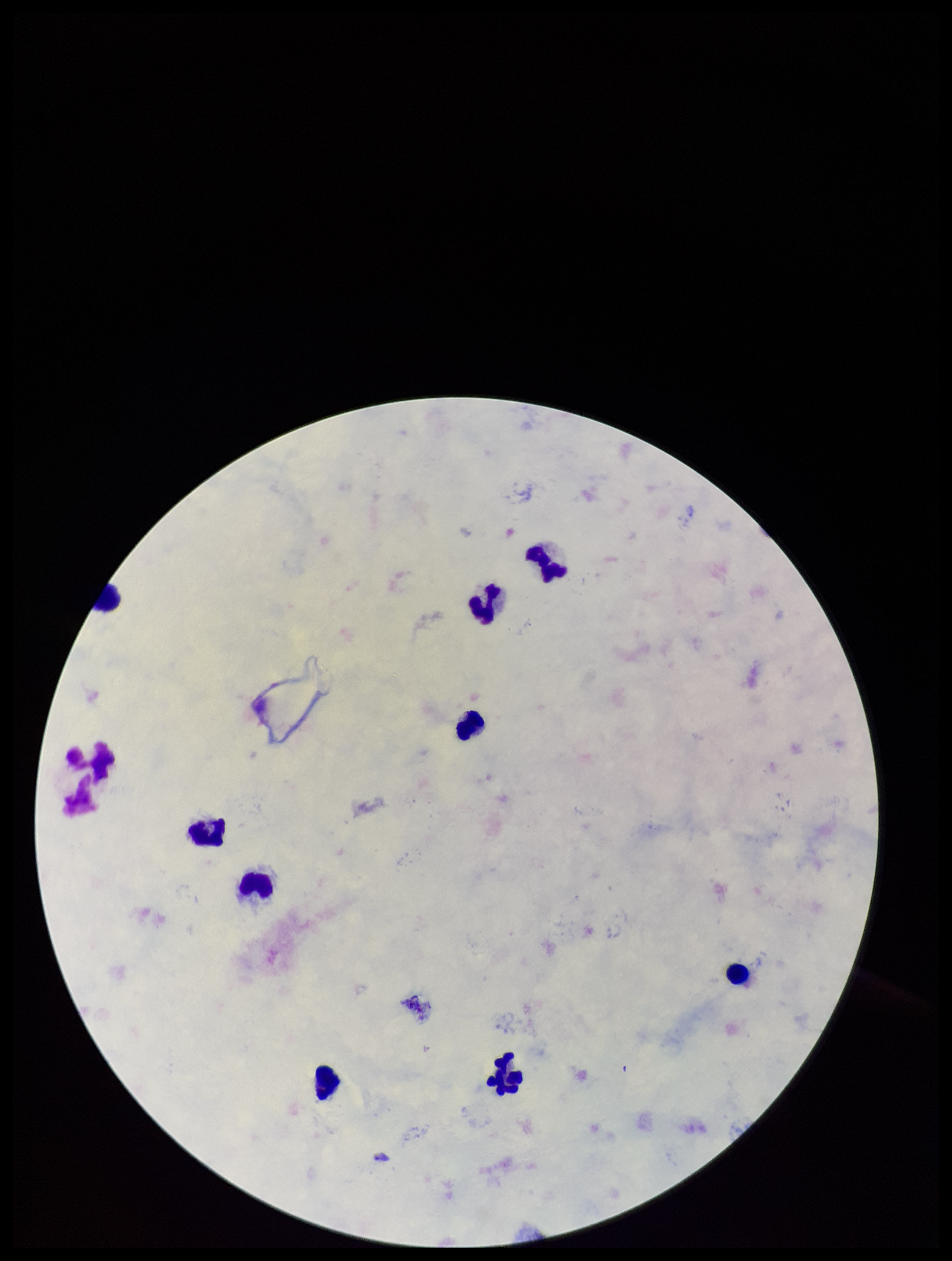
Plasmodium parasites = none seen
parasite count = 0
leukocyte count = 9
species reported for this patient = Plasmodium falciparum
capture = smartphone photograph through the microscope eyepiece
preparation = thick blood smear
image size = 952×1261 pixels
stain = Giemsa
field of view = one from this slide
patient malaria status = infected